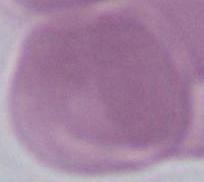
Summary:
  - Magnification: 1000x
  - Identification: red blood cell
  - Modality: photomicrograph